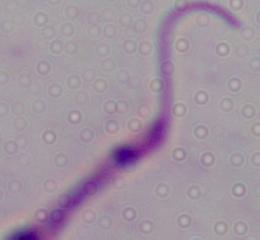

Summary:
  - Identification: Leishmania
  - Magnification: 1000x
  - Modality: photomicrograph